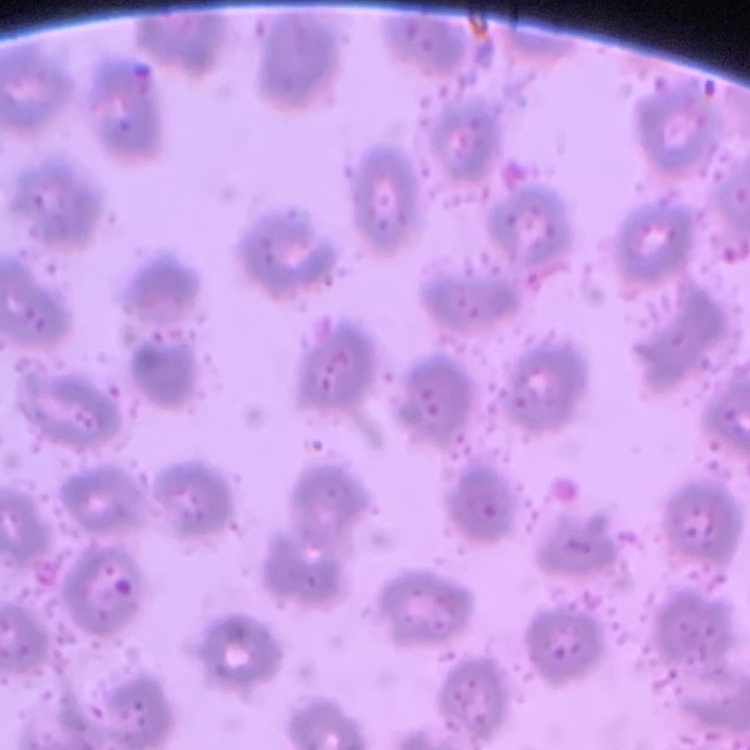
The erythrocytes show no rouleaux formation. One tile cut from a larger photomicrograph. Field's or Giemsa stain. Thin blood film.